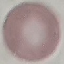

result = no malaria parasites seen
image type = cell patch, automatically extracted from a larger field of view and resized to 64 × 64 pixels
preparation = thin smear
capture = smartphone through the microscope eyepiece
stain = Giemsa